Comment on the morphology of the red blood cells.
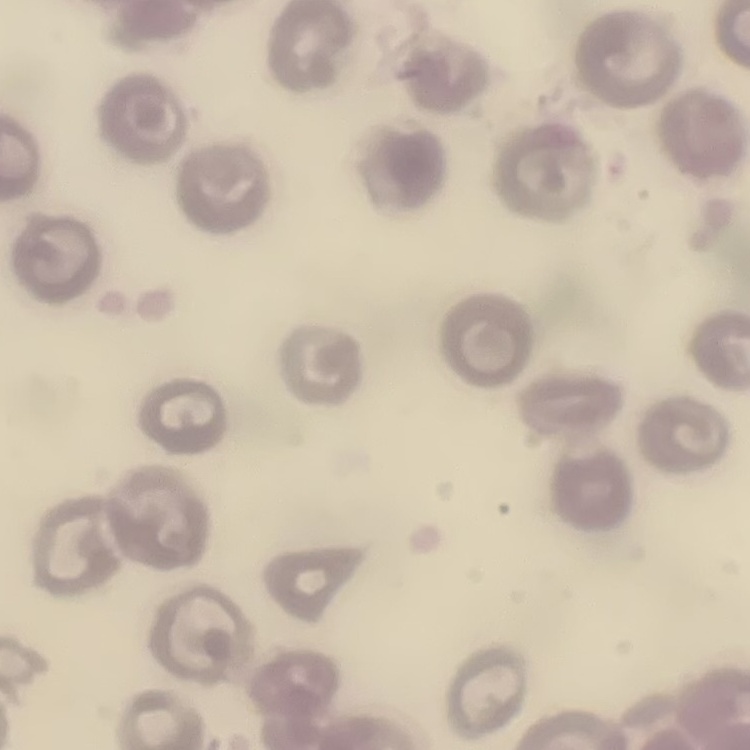
No rouleaux formation.

Stained with either Field's or Giemsa. Thin peripheral smear. One tile cut from a larger photomicrograph.